Outline each Plasmodium falciparum-infected red blood cell.
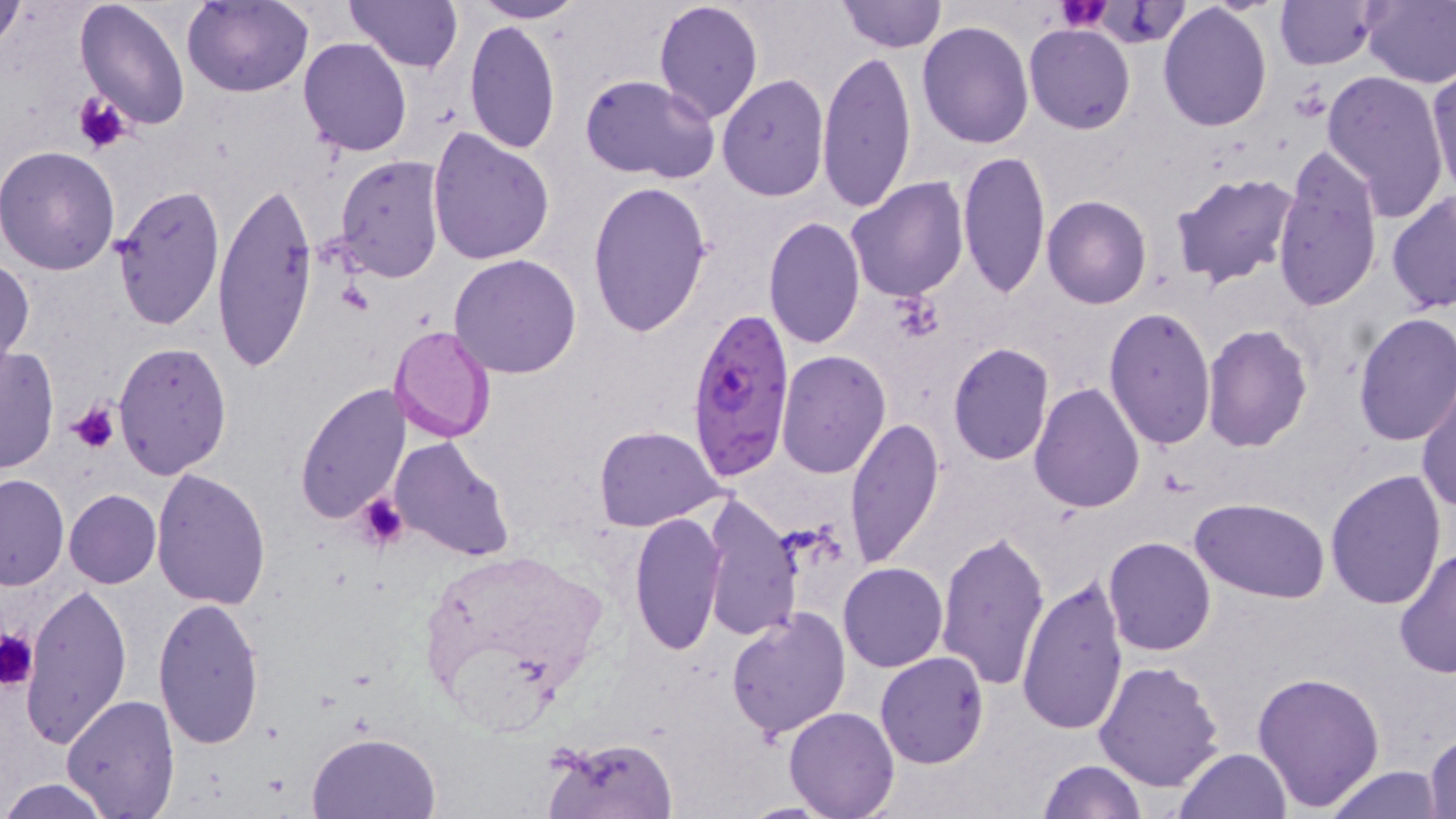

Approximate bounding boxes as (x1, y1, x2, y2) in pixels.
Plasmodium falciparum-infected red blood cells: (684, 308, 794, 477).

Uninfected red blood cell locations: (181, 0, 313, 97), (344, 0, 463, 71), (469, 0, 587, 22), (652, 0, 765, 124), (835, 0, 946, 52), (1274, 0, 1377, 71), (1359, 0, 1456, 88), (0, 1, 27, 53), (74, 1, 192, 130), (1158, 4, 1273, 131), (463, 20, 562, 155), (917, 22, 1035, 150), (1025, 23, 1134, 134), (298, 36, 413, 156), (817, 48, 919, 214), (1427, 65, 1456, 198), (1320, 70, 1450, 222), (717, 74, 828, 203), (580, 75, 719, 182), (427, 128, 555, 266), (1274, 140, 1384, 313), (0, 146, 121, 276), (958, 150, 1049, 299), (334, 155, 447, 282), (1167, 172, 1299, 290), (213, 173, 317, 375), (845, 176, 967, 302), (586, 180, 712, 337), (113, 184, 225, 332), (1386, 189, 1456, 313), (1042, 195, 1152, 309), (775, 205, 946, 338), (763, 217, 865, 352), (450, 254, 582, 377), (0, 258, 34, 372), (1103, 307, 1217, 451), (1352, 311, 1456, 448), (1201, 323, 1313, 453), (389, 324, 497, 443), (113, 343, 231, 478), (947, 343, 1055, 466), (0, 345, 58, 475), (776, 349, 890, 478), (1029, 382, 1145, 515), (295, 384, 411, 525), (1417, 384, 1456, 515), (844, 417, 944, 569), (593, 425, 724, 531), (389, 436, 515, 563), (151, 469, 272, 612), (1325, 470, 1448, 610), (0, 474, 69, 590), (64, 488, 161, 588), (698, 492, 803, 643), (1193, 498, 1331, 602), (629, 510, 729, 657), (935, 530, 1051, 692), (1103, 537, 1217, 656), (1393, 550, 1456, 678), (839, 562, 948, 672), (1016, 575, 1128, 736), (19, 580, 133, 748), (152, 597, 266, 750), (726, 605, 853, 741), (875, 652, 990, 769), (1093, 660, 1225, 793), (1251, 671, 1385, 811), (801, 686, 962, 807), (60, 694, 179, 816), (784, 707, 899, 819), (1424, 731, 1455, 818), (306, 732, 442, 819), (543, 736, 677, 819), (1174, 747, 1291, 819), (1037, 760, 1145, 819), (1323, 766, 1445, 819), (1, 777, 117, 818). Platelet locations: (1055, 1, 1110, 32), (72, 92, 133, 156), (67, 399, 122, 455), (355, 491, 412, 554), (0, 628, 37, 689). Slide-level diagnosis: Plasmodium falciparum. One field of a larger specimen. Thin blood film. Captured at 1000x magnification. Optical microscopy. Image is 1456×819 pixels. May-Grünwald-Giemsa-stained preparation.